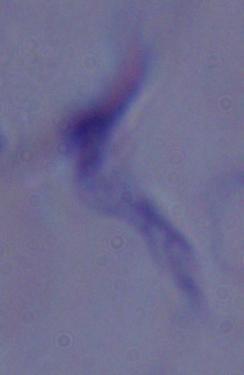

Photomicrograph. A trypanosome is shown. Captured at 1000x magnification.